Give a bounding box for every malaria parasite.
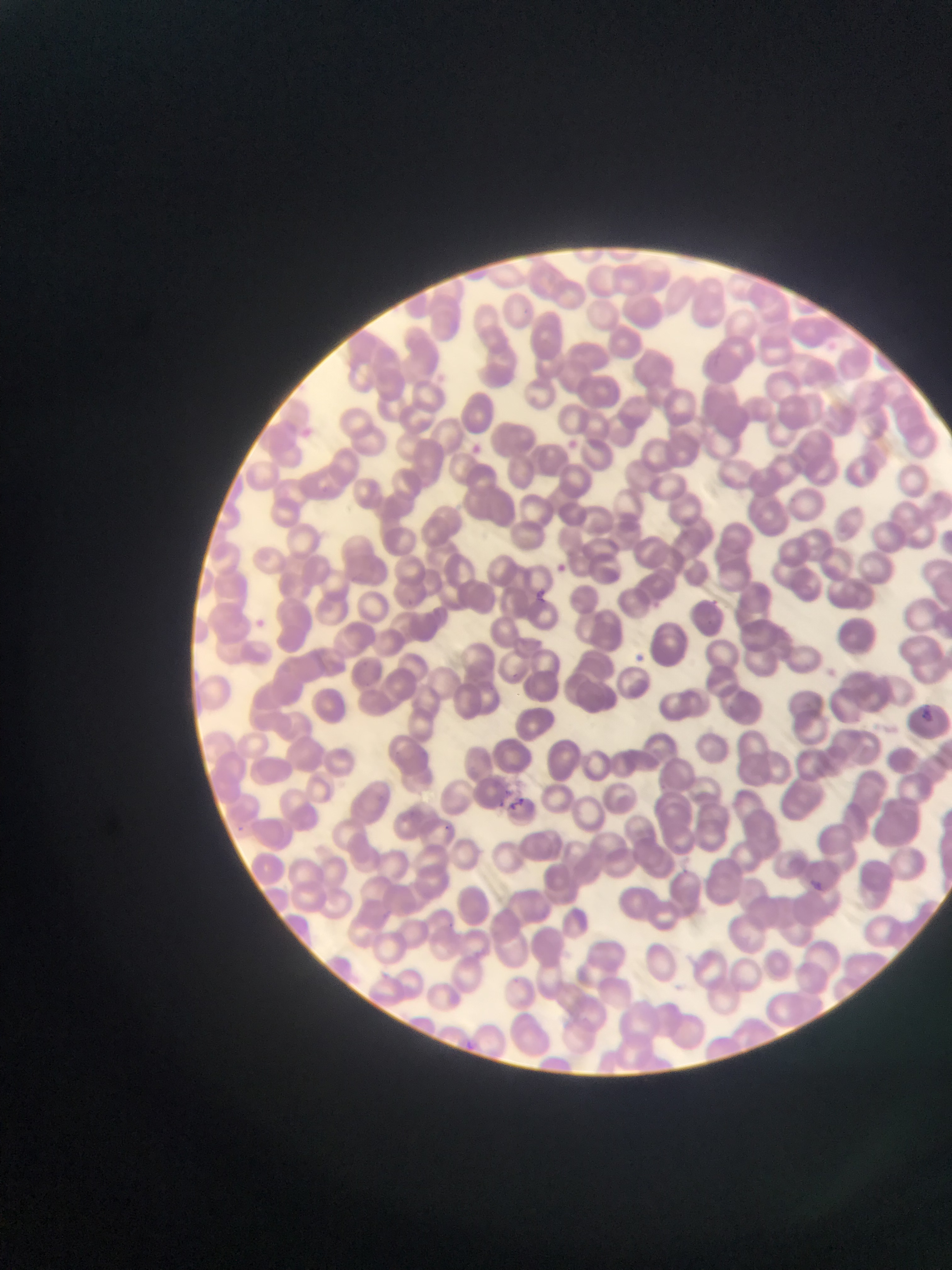
Approximate bounding boxes as left top right bottom in pixels.
Malaria parasites: 299 424 329 452; 564 437 581 454; 470 439 488 456; 549 562 575 583; 535 590 552 609; 699 592 722 610; 644 595 662 607; 249 611 274 636; 631 651 648 667; 820 660 836 679; 917 706 933 727; 501 789 529 811; 443 821 458 835; 233 822 246 839; 805 874 821 892; 464 1032 479 1044.

One field of view. Sample from Ghana. Thin blood film. Photographed through a microscope with a mobile-phone camera. Image is 952×1270 pixels.